Name the parasite shown.
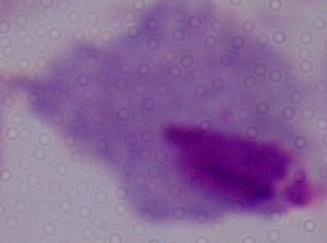
This is a trichomonad.

Summary:
  - Magnification: 1000x
  - Modality: micrograph